Name the parasite shown.
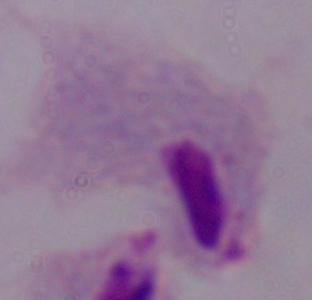
A trichomonad.

Captured at 1000x magnification. Photomicrograph.